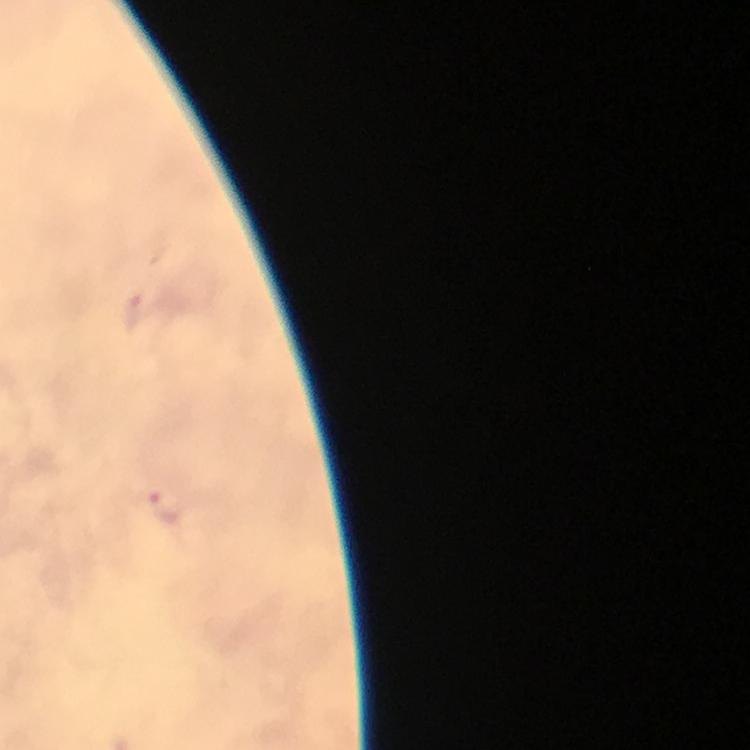 Approximate centers as [x, y] in pixels. Malaria parasite locations: [169, 505]. 100x magnification. Photographed through the microscope with a smartphone camera. Thick blood film. From a diagnostic examination for malaria. Immersion oil applied. Giemsa-stained preparation. Image is 750×750 pixels. Cropped region of a single field of view.